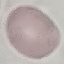

{
  "result": "negative for malaria parasites",
  "image_type": "automatically extracted cell patch, resized to 64 × 64 pixels",
  "capture": "smartphone camera at the microscope eyepiece",
  "stain": "Giemsa",
  "preparation": "thin smear"
}